Classify this cell by malaria status.
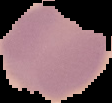

It is uninfected.

The area outside the segmented cell region is set to black. Image is 112×103 pixels. From a thin blood film.